Assess the morphology of the red blood cells.
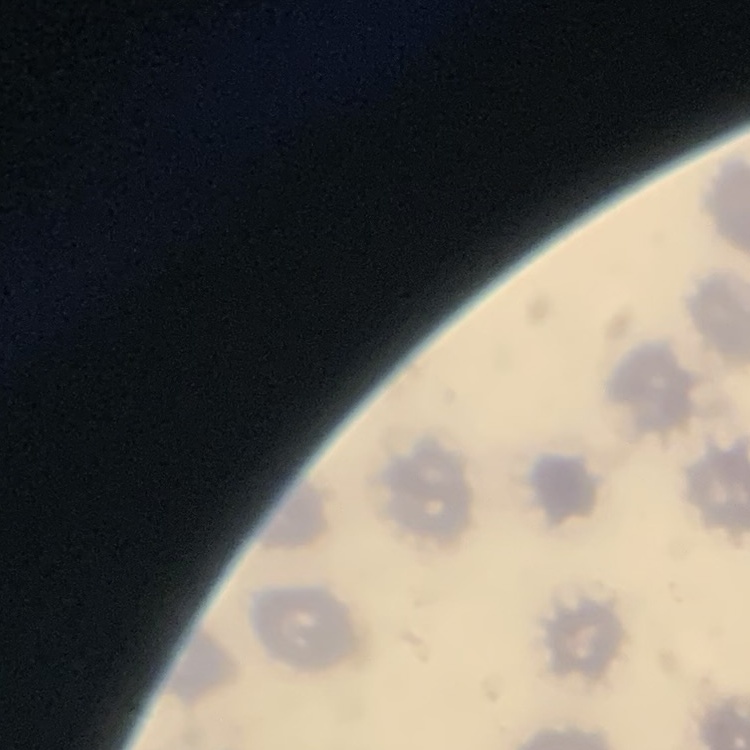
No rouleaux formation.

image_type: one tile cut from a larger photomicrograph
stain: Field's or Giemsa
preparation: thin blood smear